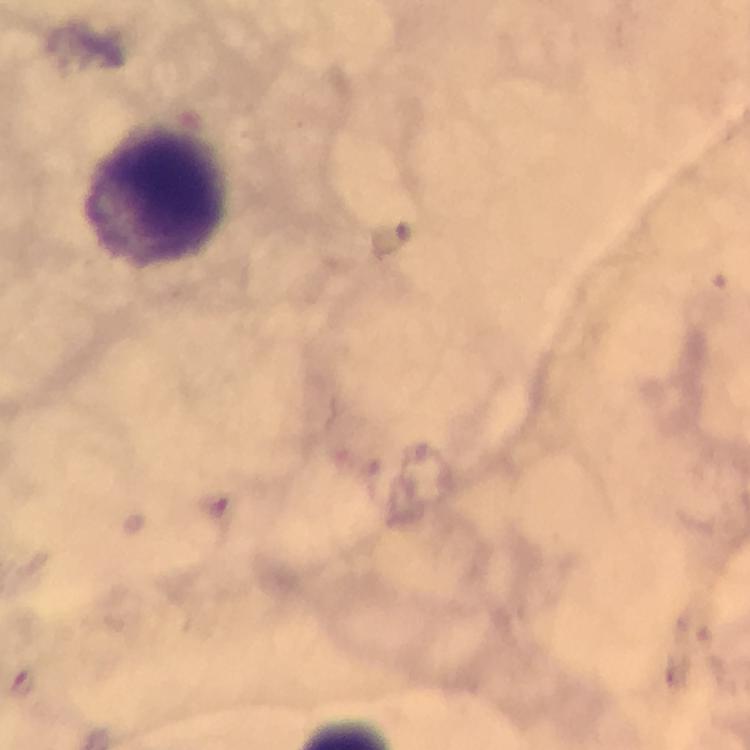

Approximate centers as (x, y) in pixels.
Summary:
  - Plasmodium parasite locations: (218, 507)
  - Leukocyte locations: (155, 193)
  - Stain: Giemsa
  - Cropped from: one field of view
  - Magnification: 100x
  - Image size: 750×750 pixels
  - Preparation: thick blood smear
  - Capture: smartphone camera through the microscope
  - Immersion oil: applied
  - Context: from a malaria diagnostic workup